Give the extent of all uninfected red blood cells.
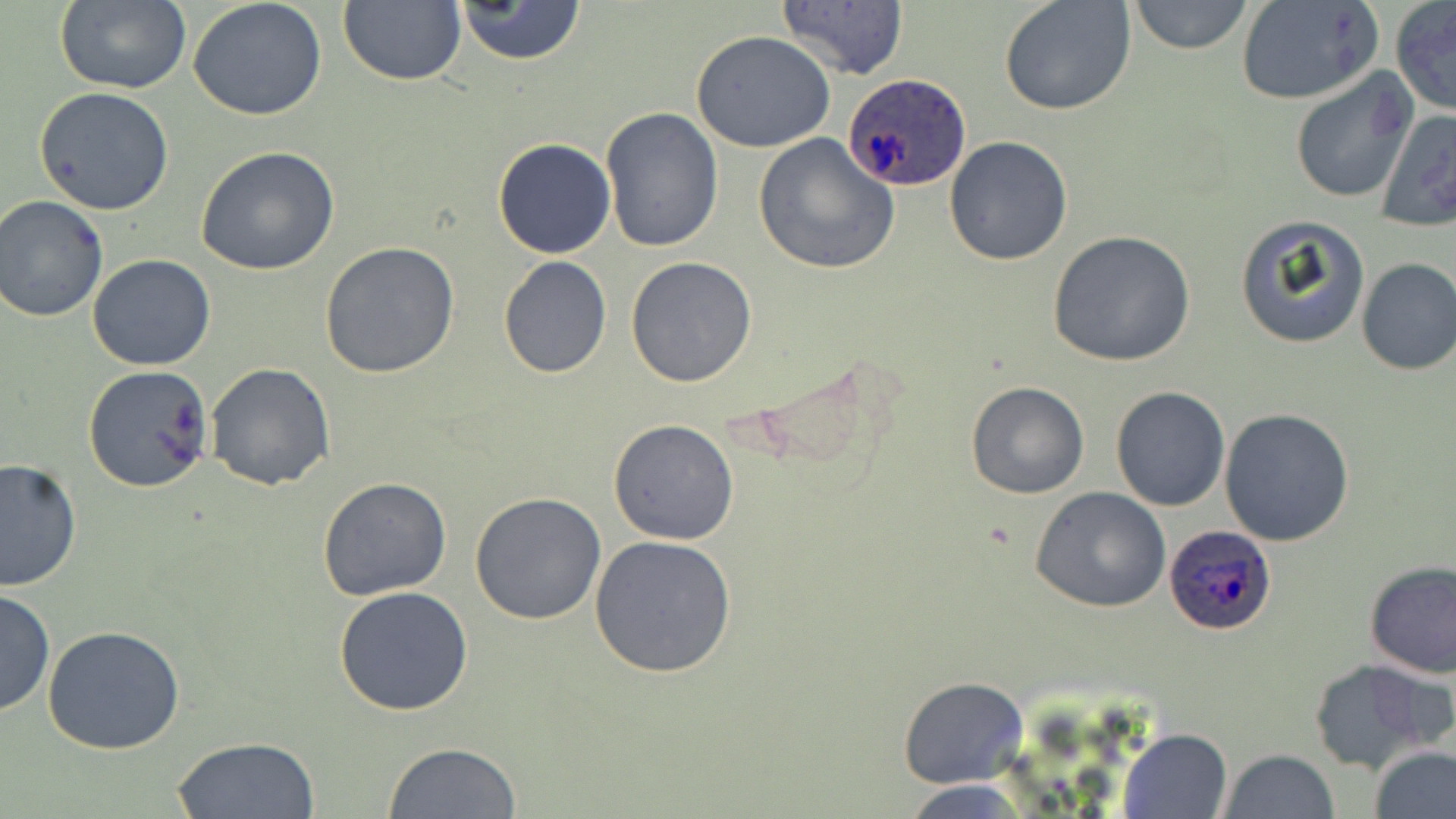
Approximate bounding boxes as (x1, y1, x2, y2) in pixels.
Uninfected red blood cells: (56, 0, 190, 94), (188, 0, 328, 122), (998, 0, 1137, 117), (1127, 0, 1254, 55), (336, 1, 467, 89), (451, 1, 589, 67), (775, 1, 909, 81), (1234, 1, 1383, 107), (1390, 2, 1456, 116), (691, 31, 839, 153), (1288, 69, 1420, 205), (34, 87, 174, 214), (601, 106, 725, 253), (1374, 107, 1456, 231), (754, 134, 898, 275), (493, 137, 617, 259), (943, 137, 1073, 266), (196, 146, 340, 276), (0, 198, 108, 322), (1233, 214, 1372, 350), (1047, 230, 1195, 368), (320, 241, 460, 379), (86, 254, 217, 371), (498, 255, 612, 377), (625, 256, 758, 389), (1356, 256, 1455, 377), (204, 362, 335, 491), (82, 364, 213, 493), (965, 381, 1090, 499), (1110, 387, 1230, 511), (1218, 407, 1355, 546), (608, 419, 739, 544), (0, 457, 80, 592), (317, 476, 453, 601), (1030, 486, 1171, 613), (469, 493, 607, 625), (588, 533, 738, 679), (1363, 560, 1456, 677), (332, 585, 476, 717), (0, 589, 55, 719), (42, 625, 187, 756), (1310, 657, 1448, 772), (899, 677, 1028, 788), (1119, 728, 1231, 818), (169, 737, 323, 819), (383, 743, 522, 819), (1370, 744, 1456, 819), (1216, 749, 1342, 819), (899, 781, 1038, 816).

Plasmodium ovale-infected red blood cell locations: (844, 72, 971, 192), (1162, 523, 1276, 635). Slide-level diagnosis: Plasmodium ovale. Thin blood film. One field of a larger specimen. Light microscopy. 1000x magnification. Image is 1456×819 pixels. May-Grünwald-Giemsa stain.